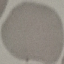
malaria_status: uninfected
stain: Giemsa
capture: smartphone through the microscope eyepiece
preparation: thin smear
image_type: automatically extracted cell patch, resized to 64 × 64 pixels